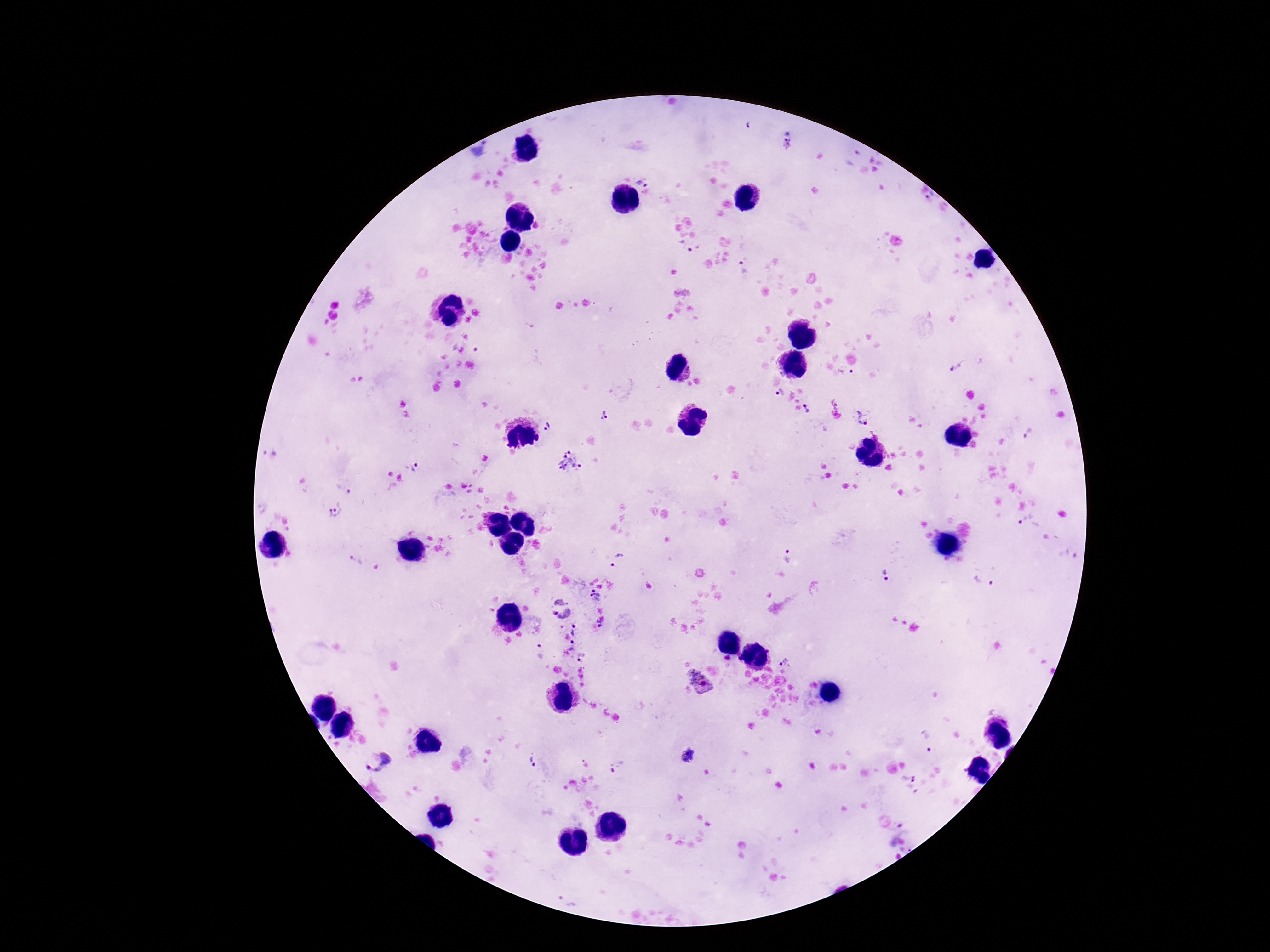
Approximate centers as [x, y] in pixels.
Summary:
  - Plasmodium parasite locations: [788, 144], [642, 183], [931, 197], [686, 246], [743, 269], [957, 366], [847, 375], [781, 394], [808, 409], [605, 416], [862, 418], [546, 427], [1027, 434], [569, 463], [414, 468], [342, 491], [335, 508], [1027, 519], [787, 556], [618, 560], [357, 562], [885, 577], [984, 580], [596, 596], [560, 602], [554, 613], [565, 614], [599, 622], [575, 630], [572, 646], [541, 650], [581, 657], [787, 660], [699, 681], [928, 741], [688, 757], [375, 761], [531, 762], [618, 767], [909, 774], [912, 792]
  - Capture: smartphone camera through the microscope eyepiece
  - Patient malaria status: infected
  - Magnification: 100x
  - Field of view: one from this slide
  - Preparation: thick peripheral-blood smear
  - Stain: Giemsa
  - Image size: 1270×952 pixels